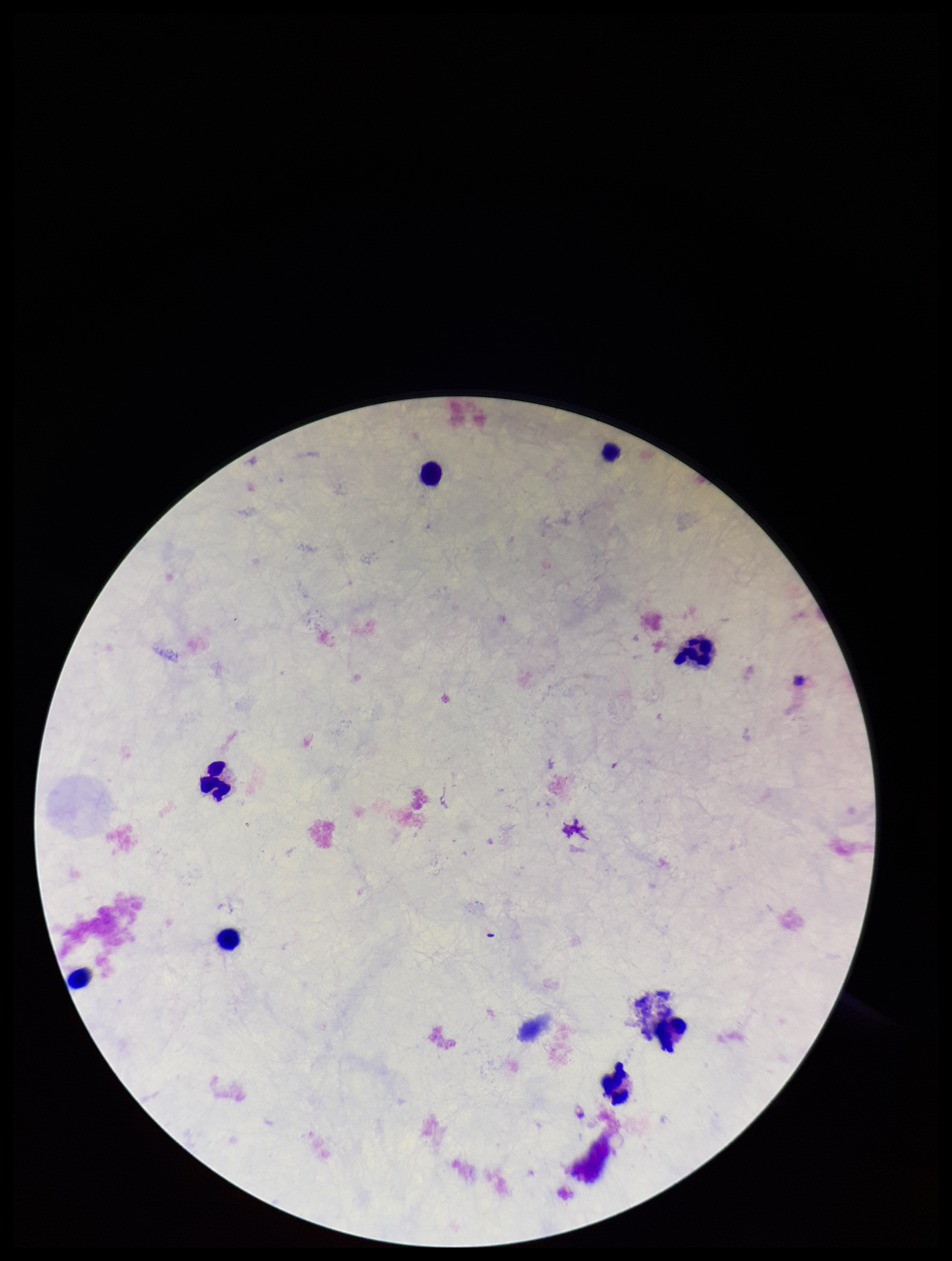

Summary:
  - Parasite count: 0
  - Patient malaria status: negative
  - Capture: smartphone photograph through the microscope eyepiece
  - Plasmodium parasites: none seen
  - Image size: 952×1261 pixels
  - Preparation: thick blood smear
  - Leukocyte count: 8
  - Stain: Giemsa
  - Field of view: one from this slide